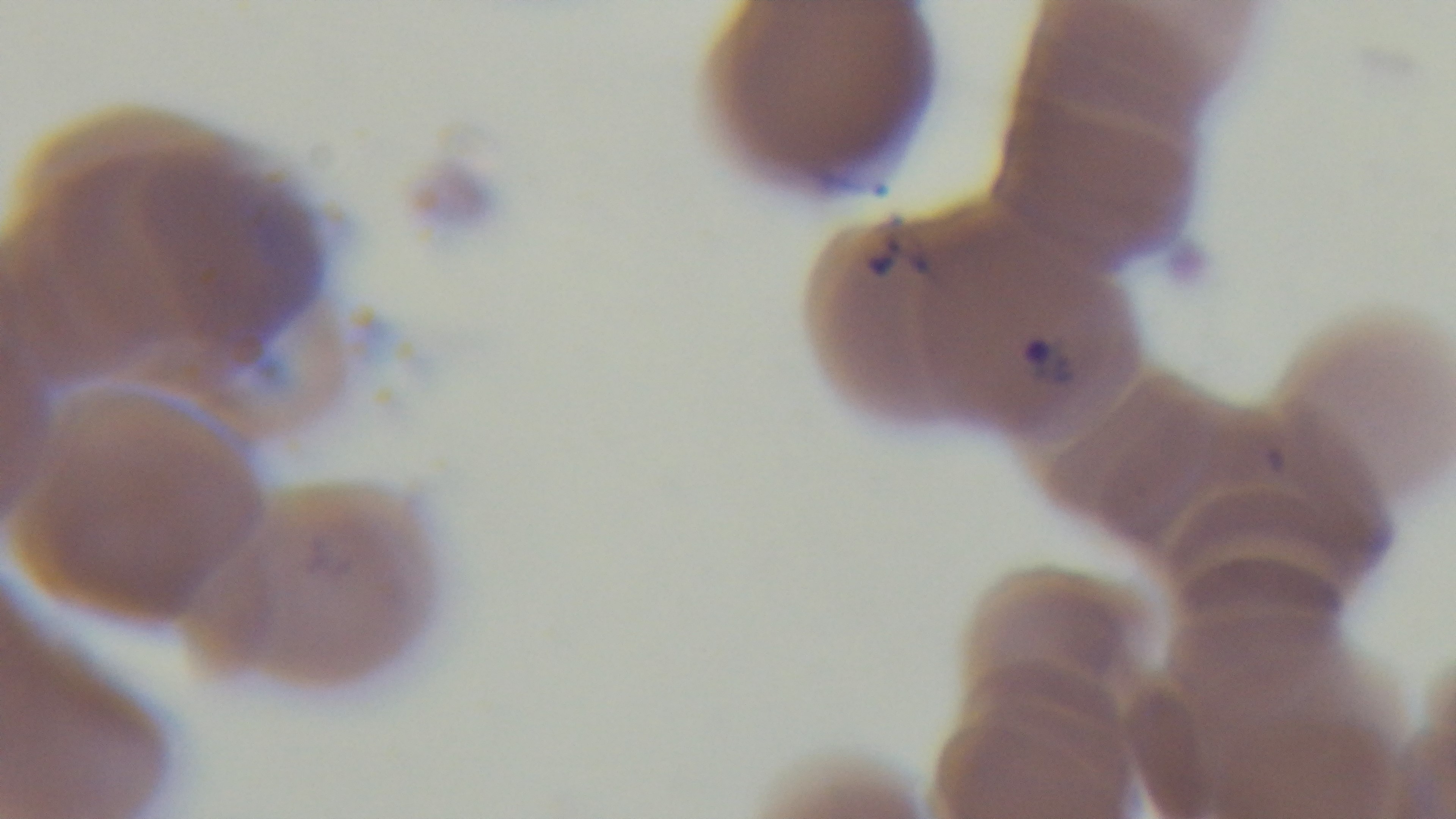

capture = mounted 4K digital camera
objective = 100x oil immersion
modality = light microscopy
malaria status = infected
stain = Giemsa
field of view = one from the slide
preparation = thin smear